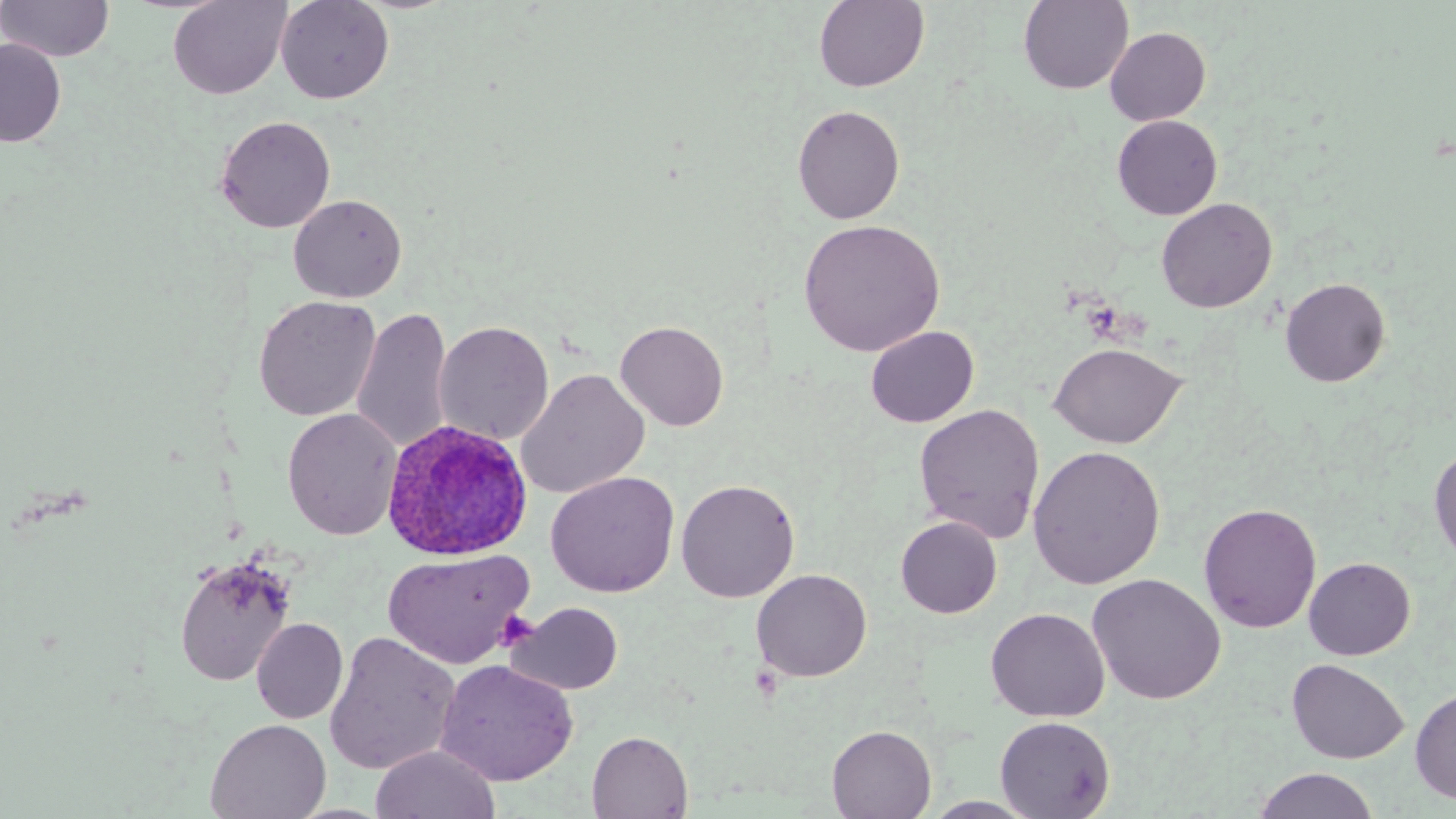
Summary:
  - Coordinate format: approximate bounding boxes as (x1, y1, x2, y2) in pixels
  - Plasmodium ovale-infected red blood cell locations: (382, 419, 532, 560)
  - Uninfected red blood cell locations: (0, 0, 114, 62), (168, 0, 292, 99), (275, 0, 394, 105), (814, 0, 929, 92), (1018, 0, 1134, 95), (1105, 26, 1211, 125), (0, 39, 66, 147), (792, 104, 905, 224), (215, 115, 336, 233), (1112, 115, 1223, 220), (288, 194, 407, 303), (1156, 197, 1277, 313), (798, 218, 945, 357), (1280, 277, 1391, 387), (253, 295, 380, 421), (351, 306, 454, 456), (614, 320, 729, 430), (434, 321, 554, 445), (865, 325, 979, 428), (1048, 342, 1186, 449), (515, 368, 650, 499), (914, 403, 1045, 543), (282, 408, 402, 541), (1429, 444, 1456, 567), (1028, 445, 1166, 589), (545, 471, 680, 598), (676, 478, 800, 602), (1198, 502, 1322, 634), (895, 516, 1002, 618), (382, 548, 535, 669), (173, 555, 296, 687), (1304, 556, 1416, 659), (752, 568, 872, 682), (1087, 572, 1226, 704), (507, 601, 624, 695), (985, 607, 1109, 722), (251, 618, 348, 724), (324, 631, 461, 776), (1287, 658, 1409, 764), (435, 659, 578, 786), (1410, 686, 1456, 804), (994, 715, 1115, 819), (205, 718, 331, 819), (827, 725, 936, 818), (587, 731, 693, 818), (370, 744, 501, 819), (1252, 768, 1381, 819), (919, 795, 1041, 818)
  - Platelet locations: (495, 615, 538, 651)
  - Slide-level diagnosis: Plasmodium ovale
  - Image size: 1456×819 pixels
  - Preparation: thin blood film
  - Modality: light microscopy
  - Stain: May-Grünwald-Giemsa
  - Field of view: single
  - Magnification: 1000x